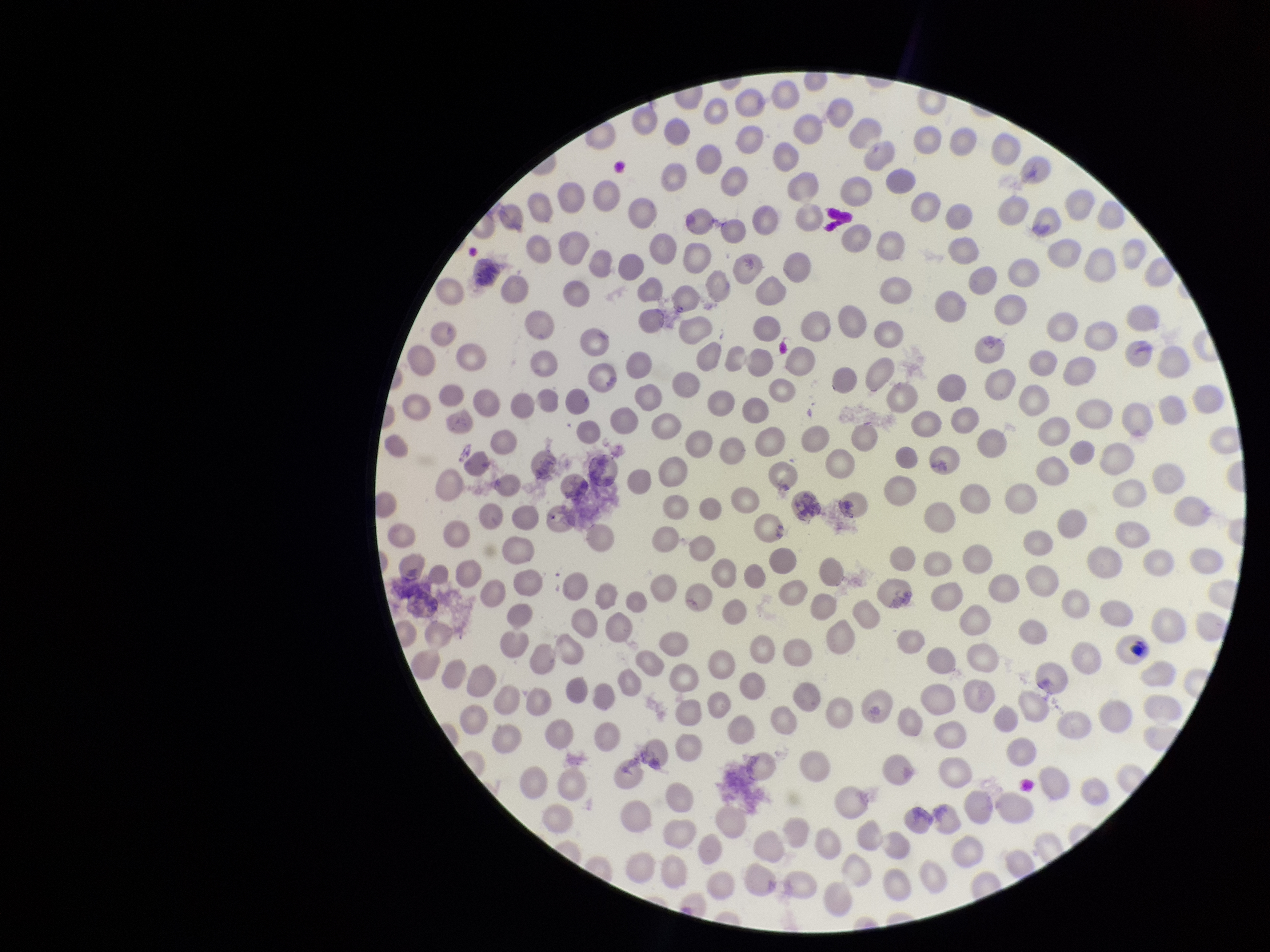

Red blood cell count: 279. Species reported for this patient: Plasmodium vivax. Preparation: thin. Photographed through the microscope eyepiece with a smartphone camera. One field from this slide. Image is 1270×952 pixels. Parasitized red blood cells: none detected. Stained with Giemsa. Parasitized red blood cell count: 0. Patient malaria status: infected.